Assess this cell for malaria.
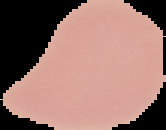

Uninfected.

Cell region segmented out of the field of view; the surrounding area is masked to black. From a thin blood film. Image is 166×130 pixels.